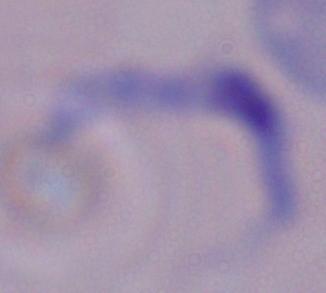
Captured at 1000x magnification. Micrograph. A trypanosome is shown.